Describe the morphology of the erythrocytes.
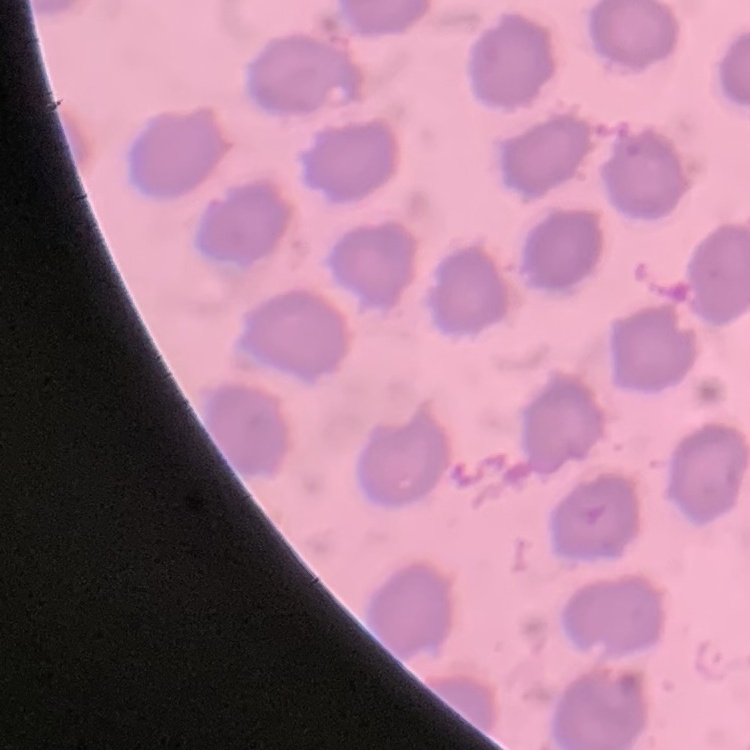
No rouleaux formation.

preparation = thin peripheral smear
image type = one tile cut from a larger photomicrograph
stain = Field's or Giemsa